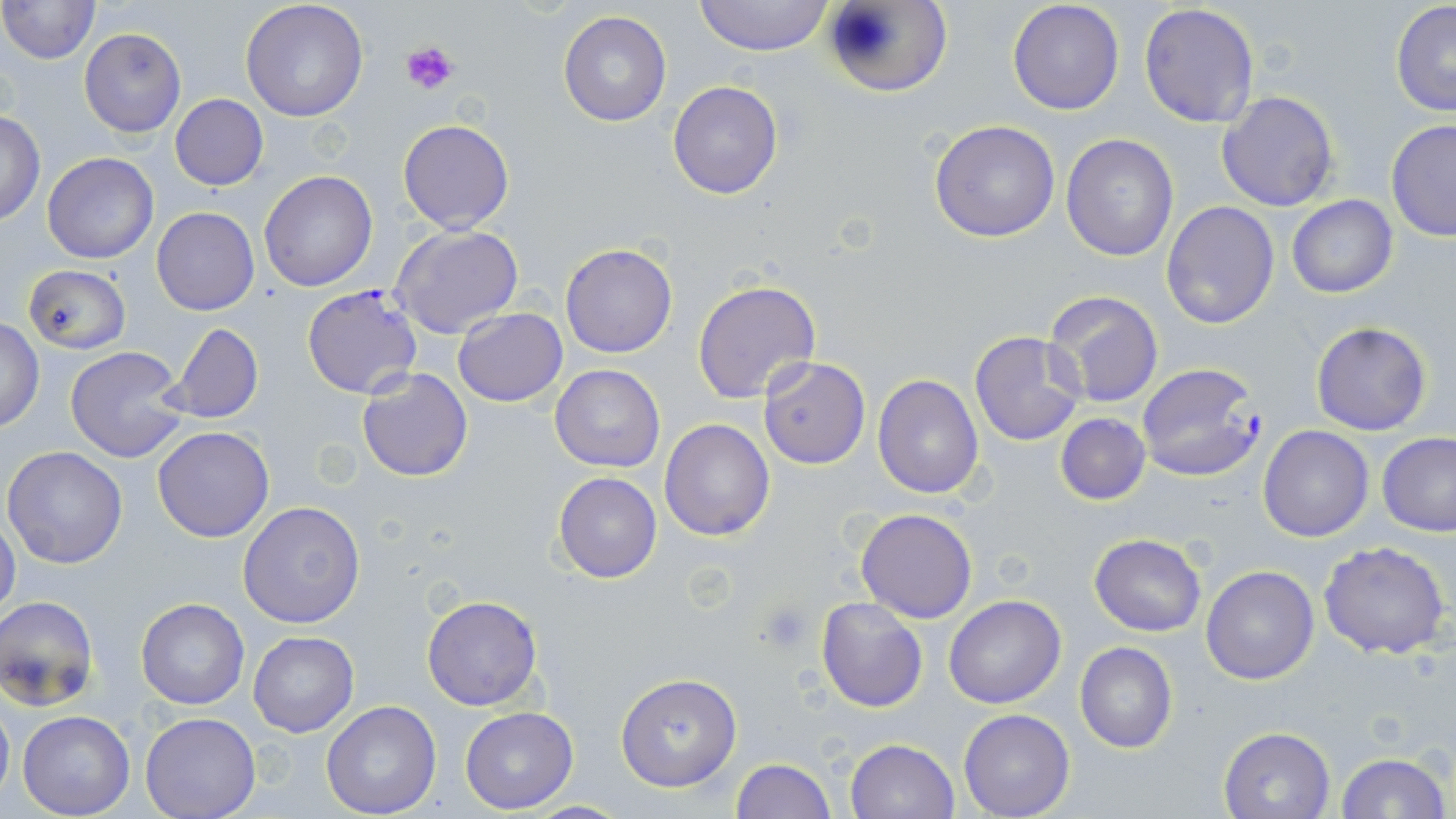
Summary:
  - Coordinate format: approximate bounding boxes as (x1, y1, x2, y2) in pixels
  - Plasmodium falciparum-infected red blood cell locations: (301, 284, 424, 399), (1136, 361, 1263, 483)
  - Platelet locations: (400, 42, 459, 95), (759, 598, 815, 653)
  - Uninfected red blood cell locations: (1, 0, 101, 65), (240, 0, 369, 121), (692, 0, 834, 56), (822, 0, 951, 98), (1007, 0, 1125, 115), (1390, 1, 1456, 117), (1138, 3, 1259, 130), (558, 11, 671, 126), (79, 28, 186, 137), (668, 80, 783, 200), (1215, 90, 1340, 212), (169, 94, 269, 190), (0, 109, 45, 226), (398, 119, 514, 234), (928, 120, 1060, 243), (1385, 120, 1456, 240), (1061, 135, 1179, 261), (42, 152, 159, 264), (259, 170, 378, 292), (1286, 195, 1398, 298), (1161, 201, 1279, 329), (152, 207, 259, 316), (391, 225, 524, 339), (559, 243, 678, 359), (24, 264, 129, 354), (693, 280, 821, 404), (1044, 290, 1165, 409), (453, 307, 566, 406), (1, 319, 45, 432), (1310, 320, 1432, 437), (168, 323, 264, 423), (969, 331, 1087, 446), (65, 347, 188, 463), (760, 357, 870, 468), (550, 363, 665, 473), (356, 369, 473, 481), (873, 373, 985, 499), (1056, 412, 1151, 506), (660, 419, 775, 540), (152, 426, 275, 543), (1258, 426, 1374, 543), (1379, 433, 1456, 537), (3, 446, 129, 568), (552, 471, 662, 584), (237, 501, 366, 629), (855, 508, 978, 623), (0, 518, 21, 625), (1089, 534, 1208, 637), (1319, 539, 1452, 659), (1201, 565, 1319, 685), (422, 595, 542, 711), (944, 595, 1067, 709), (0, 596, 100, 712), (136, 597, 249, 710), (816, 597, 927, 713), (248, 631, 358, 736), (1074, 642, 1178, 753), (615, 672, 742, 790), (0, 696, 14, 808), (321, 701, 443, 819), (459, 707, 578, 813), (957, 709, 1075, 818), (17, 710, 135, 818), (140, 713, 262, 819), (1220, 726, 1336, 818), (845, 738, 960, 819), (1334, 750, 1452, 819), (731, 758, 836, 819), (519, 800, 634, 817)
  - Slide-level diagnosis: Plasmodium falciparum
  - Image size: 1456×819 pixels
  - Preparation: thin blood smear
  - Modality: light microscopy
  - Field of view: one of a larger specimen
  - Magnification: 1000x
  - Stain: May-Grünwald-Giemsa